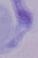
{
  "modality": "photomicrograph",
  "magnification": "1000x",
  "identification": "trypanosome"
}